Locate and identify every blood parasite.
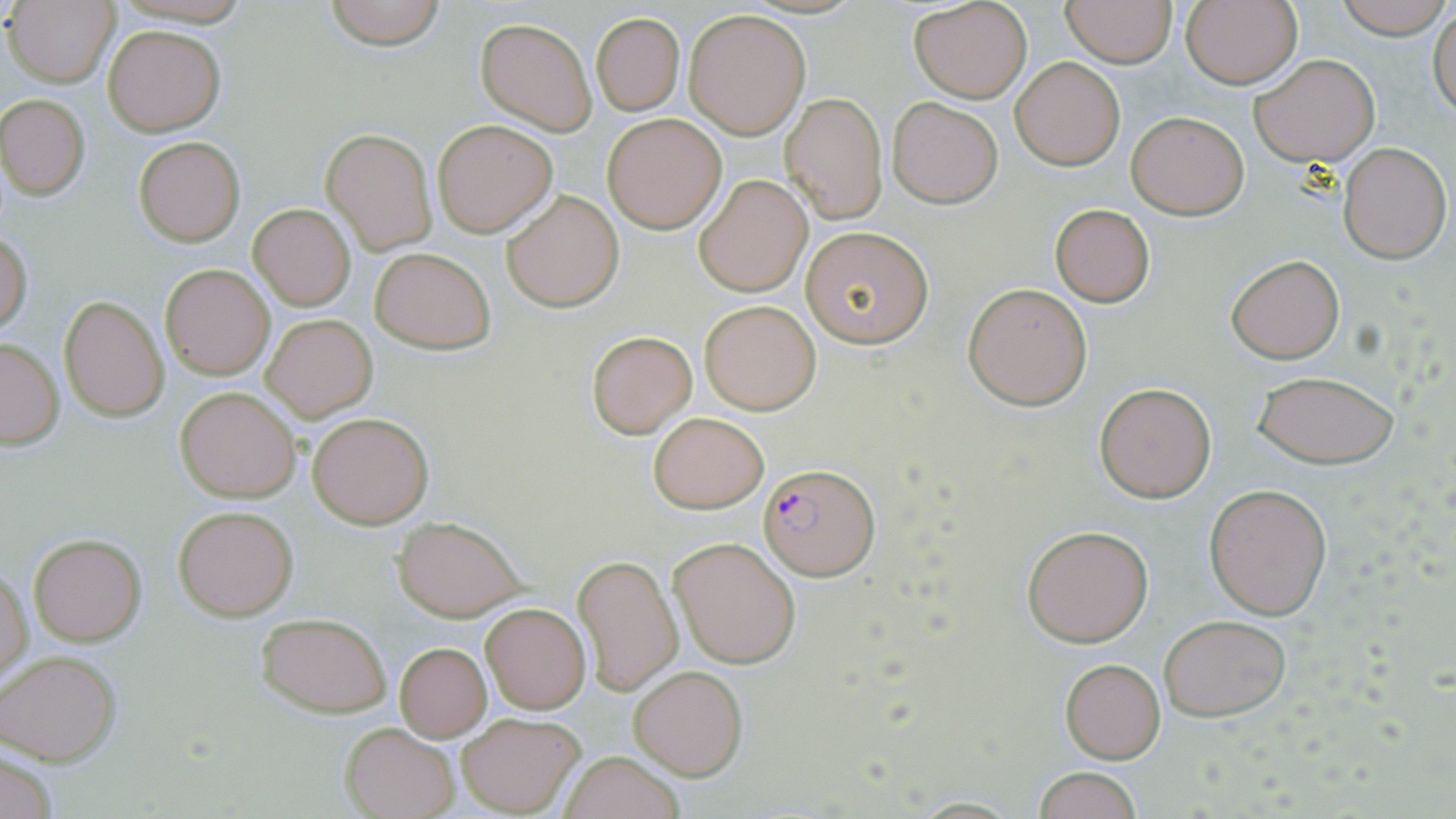

Approximate bounding boxes as [x1, y1, x2, y2] in pixels.
Plasmodium falciparum-infected red blood cells: [758, 461, 879, 581].
No Plasmodium ovale, Plasmodium malariae, Plasmodium vivax, Babesia divergens, or Trypanosoma brucei observed.

Summary:
  - Uninfected red blood cell locations: [321, 0, 450, 50], [1182, 0, 1303, 90], [1335, 0, 1451, 40], [1061, 1, 1176, 67], [7, 2, 118, 85], [908, 2, 1033, 103], [1430, 7, 1456, 120], [683, 8, 812, 140], [591, 13, 684, 117], [476, 18, 597, 134], [104, 25, 224, 135], [1250, 53, 1379, 167], [1010, 57, 1125, 170], [782, 92, 888, 224], [1, 94, 90, 200], [888, 97, 1003, 208], [1126, 109, 1250, 219], [602, 113, 727, 232], [433, 119, 557, 236], [321, 128, 436, 255], [134, 136, 245, 246], [1336, 141, 1451, 264], [693, 173, 813, 298], [502, 189, 624, 312], [249, 203, 355, 310], [1049, 203, 1155, 308], [800, 226, 933, 348], [0, 232, 32, 336], [370, 247, 496, 353], [1225, 253, 1345, 364], [160, 264, 275, 380], [962, 282, 1093, 410], [60, 294, 169, 422], [699, 300, 821, 414], [262, 313, 378, 421], [585, 330, 698, 437], [0, 337, 64, 448], [1253, 370, 1400, 468], [1095, 382, 1215, 501], [176, 387, 300, 503], [306, 410, 434, 528], [649, 411, 769, 514], [1205, 482, 1332, 621], [174, 505, 298, 620], [393, 516, 522, 620], [1022, 525, 1153, 646], [28, 534, 146, 646], [668, 537, 801, 668], [574, 555, 682, 695], [1, 561, 32, 685], [480, 602, 591, 714], [257, 612, 391, 715], [1158, 614, 1292, 721], [392, 642, 492, 741], [0, 650, 122, 764], [1059, 658, 1165, 763], [629, 666, 747, 780], [456, 711, 585, 816], [342, 722, 459, 819], [1, 749, 59, 819], [559, 751, 684, 819], [1030, 766, 1146, 819]
  - Slide-level diagnosis: Plasmodium falciparum
  - Preparation: thin blood smear
  - Modality: optical microscopy
  - Field of view: single
  - Magnification: 1000x
  - Stain: May-Grünwald-Giemsa
  - Image size: 1456×819 pixels